Name the cell type shown.
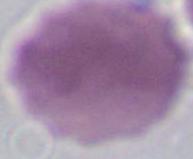
An erythrocyte.

modality = micrograph
magnification = 1000x